Classify this cell by malaria status.
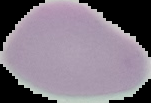
It is uninfected.

Cell region segmented out of the field of view; the surrounding area is masked to black. Image is 151×103 pixels. From a thin blood film.